Locate and identify every blood parasite.
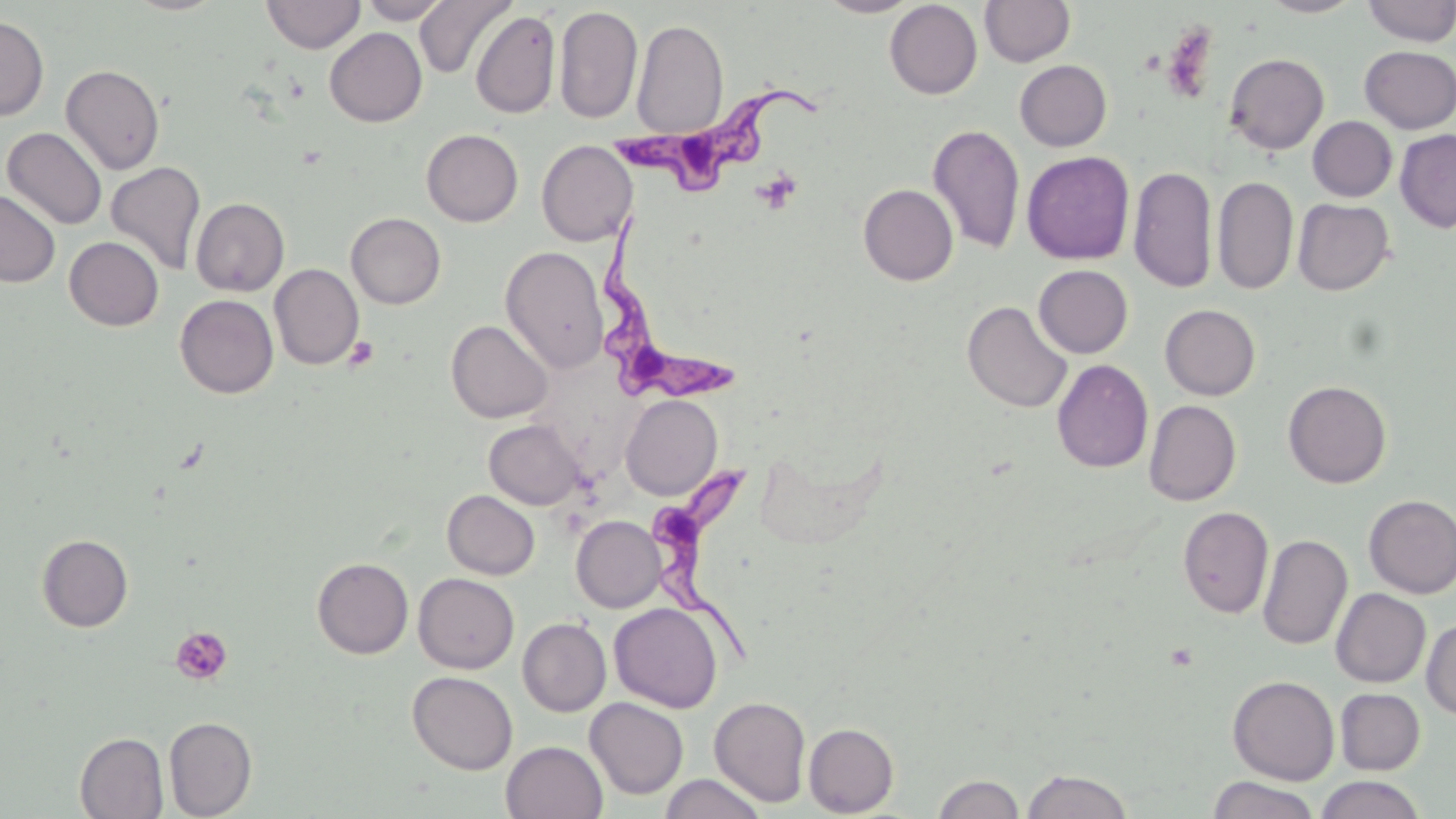
Approximate bounding boxes as [x1, y1, x2, y2] in pixels.
Trypanosoma brucei: [618, 82, 824, 203], [599, 214, 731, 406], [647, 451, 770, 666].
No Plasmodium falciparum, Plasmodium ovale, Plasmodium malariae, Plasmodium vivax, or Babesia divergens observed.

slide_level_diagnosis: Trypanosoma brucei
platelet_locations: 'approximate bounding boxes as [x1, y1, x2, y2] in pixels: [1161, 23, 1219, 103], [755, 169, 801, 213], [345, 336, 379, 370], [170, 626, 233, 685]'
preparation: thin blood smear
modality: optical microscopy
uninfected_red_blood_cell_locations: 'approximate bounding boxes as [x1, y1, x2, y2] in pixels: [261, 0, 365, 54], [358, 0, 454, 24], [415, 0, 515, 80], [817, 0, 921, 17], [979, 0, 1075, 67], [1260, 0, 1364, 17], [884, 1, 982, 99], [1361, 1, 1456, 46], [554, 6, 642, 123], [471, 10, 560, 119], [0, 16, 49, 121], [632, 19, 728, 138], [324, 27, 427, 127], [1358, 45, 1456, 133], [1224, 52, 1330, 155], [1014, 60, 1112, 151], [60, 64, 165, 175], [1307, 116, 1397, 202], [926, 123, 1025, 255], [3, 127, 106, 230], [1395, 128, 1456, 233], [421, 129, 523, 226], [536, 140, 637, 246], [1021, 151, 1135, 265], [106, 162, 206, 276], [1128, 165, 1218, 293], [1212, 175, 1298, 296], [858, 184, 958, 286], [0, 191, 60, 287], [191, 198, 289, 296], [1292, 198, 1394, 295], [345, 212, 446, 309], [64, 236, 164, 330], [500, 245, 609, 375], [269, 264, 364, 369], [1033, 264, 1133, 358], [175, 294, 278, 398], [962, 300, 1072, 413], [1160, 304, 1260, 400], [446, 320, 553, 423], [1052, 359, 1153, 473], [1283, 380, 1391, 488], [621, 395, 722, 500], [1144, 400, 1241, 506], [484, 419, 586, 510], [442, 490, 539, 579], [1363, 495, 1456, 598], [1178, 506, 1274, 618], [571, 515, 666, 612], [36, 534, 133, 632], [1257, 534, 1352, 651], [312, 557, 414, 658], [413, 573, 519, 674], [1331, 588, 1431, 688], [609, 603, 724, 713], [518, 617, 612, 716], [1421, 617, 1456, 720], [408, 671, 517, 775], [1227, 675, 1340, 785], [1335, 688, 1425, 775], [709, 695, 811, 807], [585, 697, 688, 799], [585, 698, 813, 802], [163, 716, 257, 818], [804, 723, 899, 817], [75, 732, 168, 818], [501, 740, 607, 819], [1021, 769, 1133, 818], [660, 773, 766, 819], [932, 773, 1025, 818], [1315, 775, 1427, 819], [1207, 776, 1321, 818]'
image_size: 1456×819 pixels
stain: May-Grünwald-Giemsa
field_of_view: single
magnification: 1000x